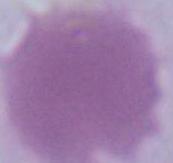
Captured at 1000x magnification. An erythrocyte is shown. Photomicrograph.